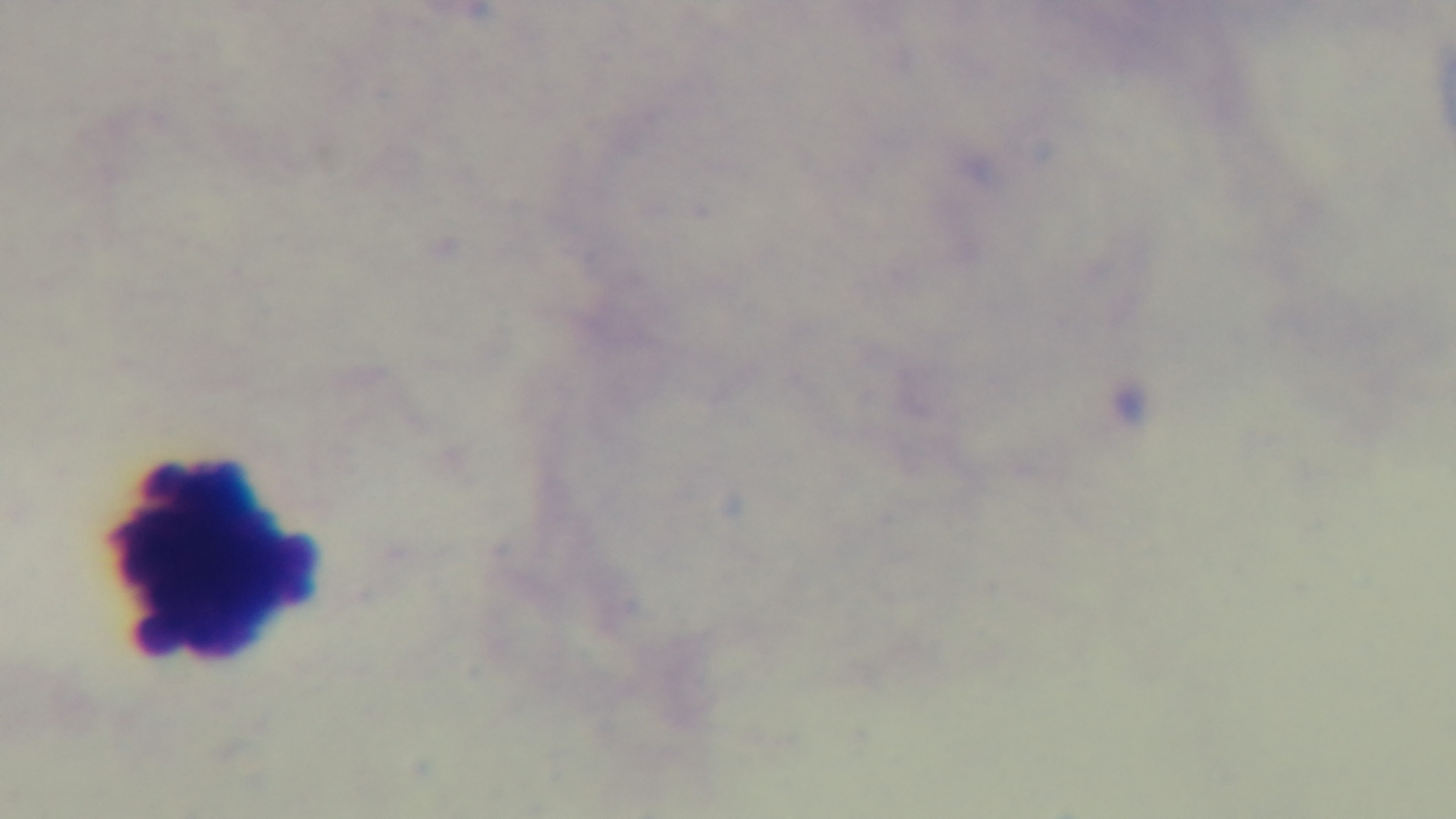

Summary:
  - Preparation: thick
  - Modality: light microscopy
  - Capture: mounted 4K digital camera
  - Objective: 100x oil immersion
  - Stain: Giemsa
  - Field of view: one from the slide
  - Malaria status: negative